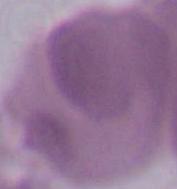 Micrograph. An erythrocyte is shown. 1000x magnification.